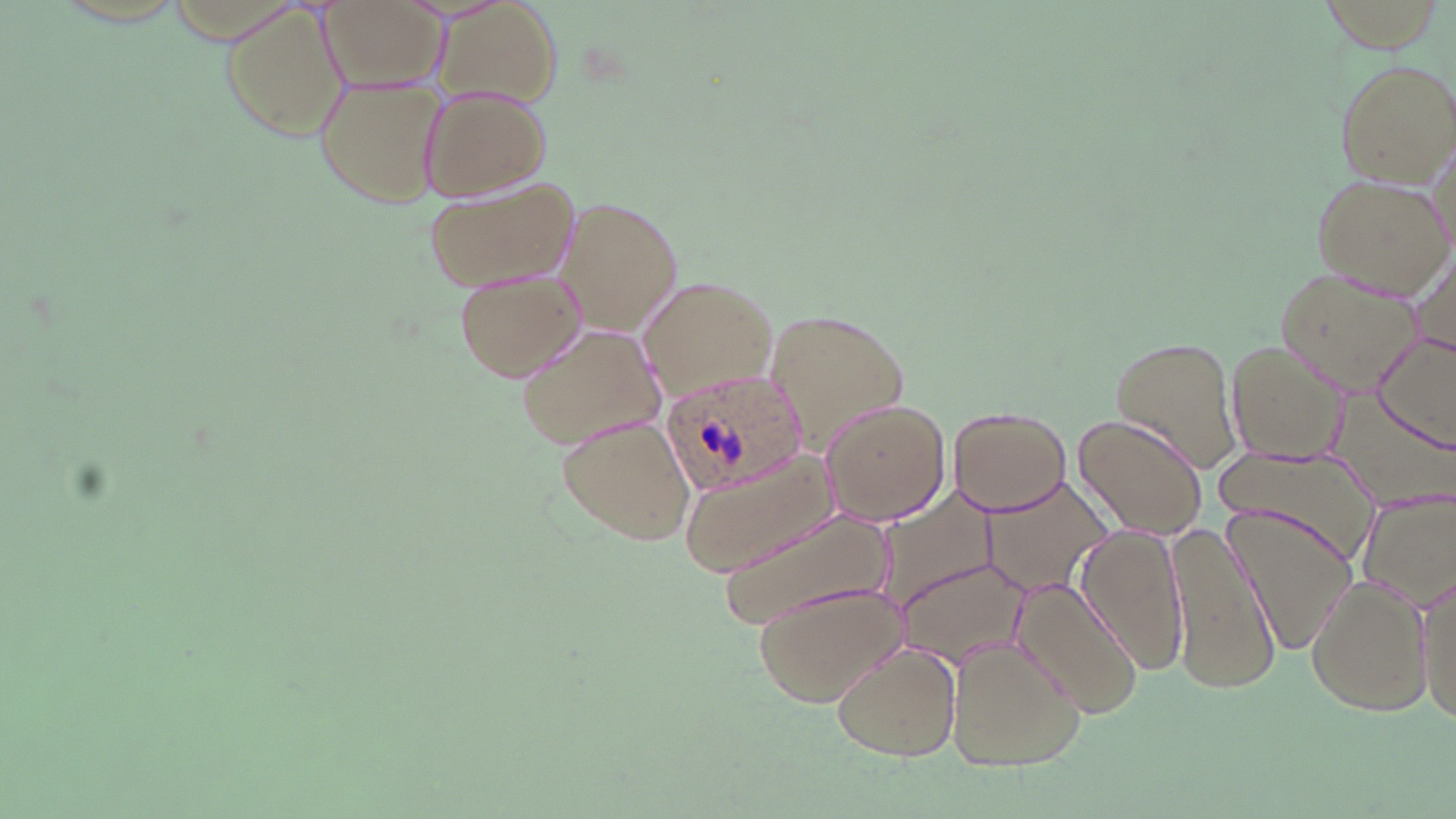

Summary:
  - Coordinate format: approximate bounding boxes as (x1, y1, x2, y2) in pixels
  - Plasmodium ovale-infected red blood cell locations: (660, 369, 808, 500)
  - Uninfected red blood cell locations: (317, 0, 445, 97), (435, 2, 561, 107), (220, 4, 347, 141), (1334, 57, 1456, 185), (316, 74, 447, 207), (419, 87, 551, 200), (1310, 173, 1452, 300), (425, 176, 577, 292), (554, 199, 680, 333), (1403, 232, 1456, 359), (1278, 263, 1429, 396), (455, 268, 586, 383), (639, 277, 779, 400), (763, 304, 911, 450), (517, 320, 666, 450), (1372, 333, 1456, 451), (1110, 335, 1243, 475), (1224, 338, 1349, 462), (1329, 388, 1456, 510), (819, 397, 952, 526), (948, 404, 1073, 515), (1073, 410, 1210, 538), (557, 414, 699, 547), (1214, 444, 1377, 565), (680, 450, 833, 575), (979, 475, 1114, 597), (865, 484, 1002, 622), (1356, 486, 1456, 612), (712, 504, 901, 626), (1224, 504, 1357, 659), (1166, 520, 1282, 696), (1073, 523, 1191, 674), (894, 558, 1028, 670), (1306, 572, 1430, 718), (1416, 573, 1454, 730), (1010, 578, 1144, 718), (754, 579, 906, 707), (944, 637, 1087, 773), (831, 642, 962, 761)
  - Slide-level diagnosis: Plasmodium ovale
  - Magnification: 1000x
  - Stain: May-Grünwald-Giemsa
  - Field of view: one of a larger specimen
  - Preparation: thin blood smear
  - Image size: 1456×819 pixels
  - Modality: optical microscopy